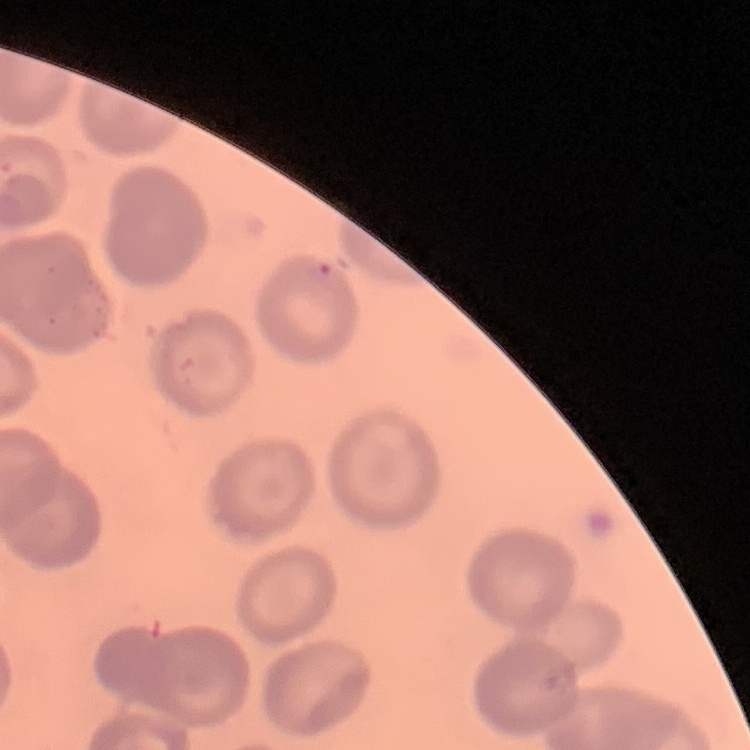

Summary:
  - Red blood cell morphology: no rouleaux formation
  - Image type: square crop of a larger photomicrograph
  - Stain: Field's or Giemsa
  - Preparation: thin blood film